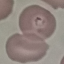
Result: malaria parasites identified. Thin smear of blood. Acquired by smartphone through the microscope eyepiece. Cell patch, automatically extracted from a larger field of view and resized to 64 × 64 pixels. Giemsa stain.